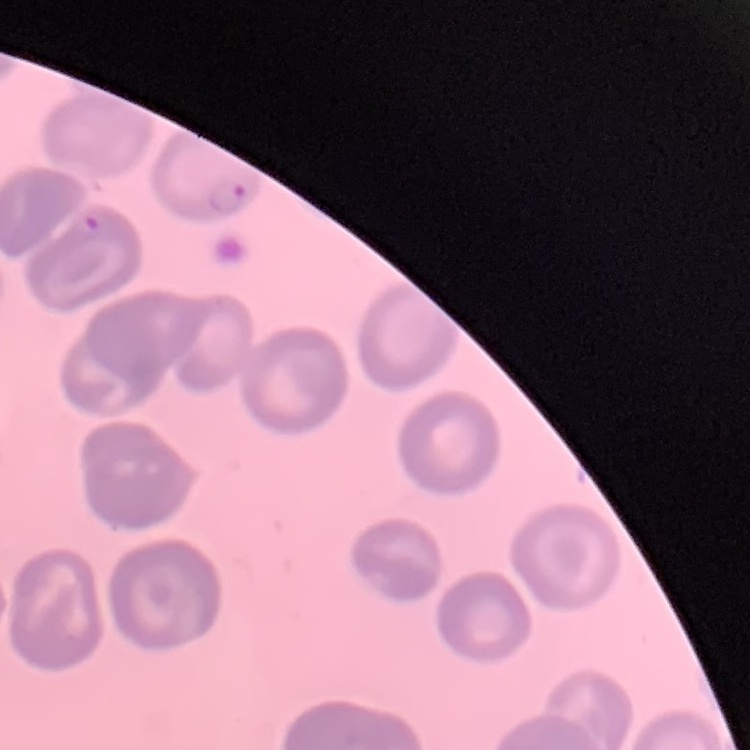

erythrocyte morphology = no rouleaux formation
stain = Field's or Giemsa
image type = one tile cut from a larger photomicrograph
preparation = thin peripheral smear